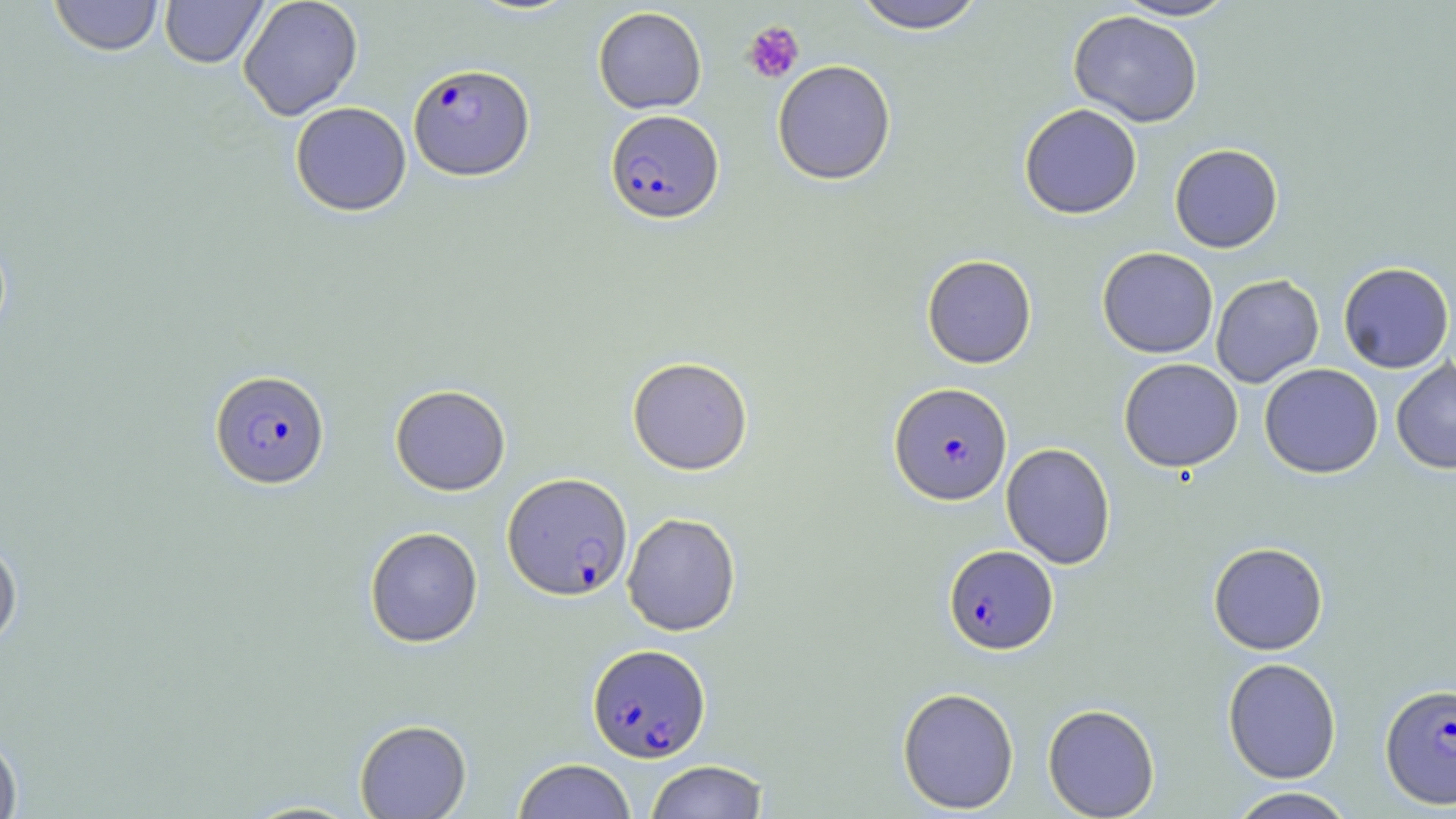
slide-level diagnosis = Plasmodium falciparum
image size = 1456×819 pixels
platelet locations = approximate bounding boxes as named x1/y1/x2/y2 corners in pixels: (x1=742, y1=21, x2=804, y2=84)
stain = May-Grünwald-Giemsa
modality = light microscopy
field of view = single
uninfected red blood cell locations = approximate bounding boxes as named x1/y1/x2/y2 corners in pixels: (x1=48, y1=0, x2=164, y2=57), (x1=159, y1=0, x2=269, y2=68), (x1=238, y1=0, x2=364, y2=120), (x1=850, y1=0, x2=987, y2=33), (x1=1112, y1=0, x2=1240, y2=21), (x1=593, y1=6, x2=707, y2=114), (x1=1068, y1=10, x2=1203, y2=127), (x1=772, y1=60, x2=896, y2=185), (x1=289, y1=101, x2=411, y2=216), (x1=1019, y1=103, x2=1142, y2=219), (x1=1169, y1=144, x2=1283, y2=253), (x1=1097, y1=247, x2=1219, y2=358), (x1=922, y1=254, x2=1037, y2=368), (x1=1338, y1=262, x2=1455, y2=373), (x1=1211, y1=274, x2=1324, y2=388), (x1=627, y1=356, x2=753, y2=475), (x1=1119, y1=358, x2=1243, y2=472), (x1=1391, y1=359, x2=1456, y2=474), (x1=1259, y1=363, x2=1384, y2=478), (x1=390, y1=384, x2=511, y2=496), (x1=1001, y1=442, x2=1116, y2=569), (x1=622, y1=512, x2=741, y2=636), (x1=364, y1=526, x2=483, y2=648), (x1=0, y1=536, x2=23, y2=650), (x1=1208, y1=542, x2=1328, y2=655), (x1=1222, y1=657, x2=1342, y2=783), (x1=897, y1=686, x2=1020, y2=814), (x1=1043, y1=703, x2=1160, y2=818), (x1=354, y1=719, x2=471, y2=818), (x1=0, y1=730, x2=23, y2=819), (x1=513, y1=758, x2=636, y2=818), (x1=644, y1=760, x2=769, y2=819), (x1=1227, y1=787, x2=1357, y2=818)
magnification = 1000x
Plasmodium falciparum-infected red blood cell locations = approximate bounding boxes as named x1/y1/x2/y2 corners in pixels: (x1=408, y1=63, x2=534, y2=180), (x1=605, y1=109, x2=724, y2=224), (x1=209, y1=369, x2=330, y2=488), (x1=889, y1=382, x2=1012, y2=504), (x1=502, y1=472, x2=633, y2=601), (x1=943, y1=545, x2=1058, y2=654), (x1=587, y1=643, x2=710, y2=762), (x1=1380, y1=682, x2=1456, y2=810)
preparation = thin blood smear